Identify the cell.
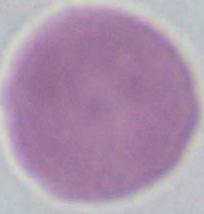

This is an erythrocyte.

modality = photomicrograph
magnification = 1000x